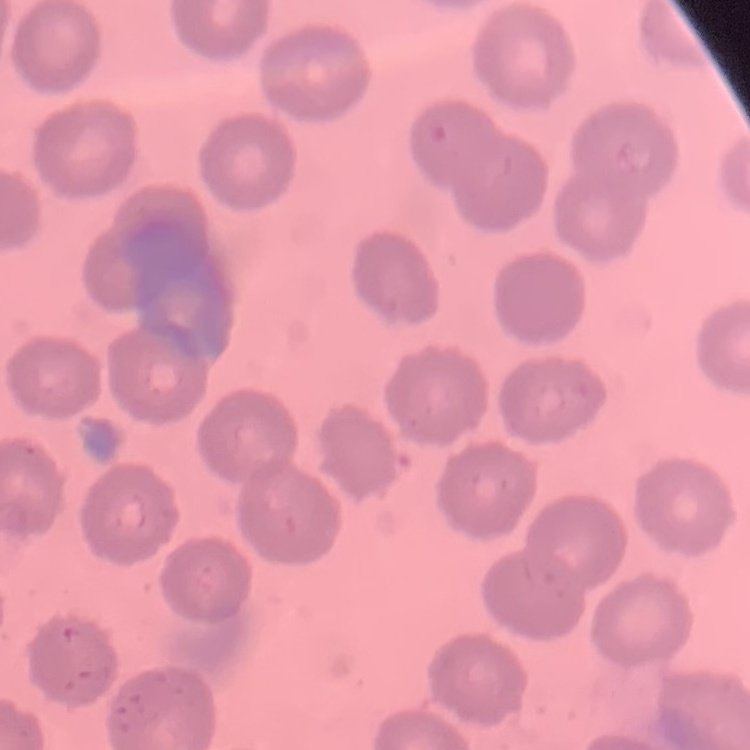

{
  "erythrocyte_morphology": "no rouleaux formation",
  "image_type": "one tile cut from a larger photomicrograph",
  "preparation": "thin blood smear",
  "stain": "Field's or Giemsa"
}